Describe the morphology of the erythrocytes.
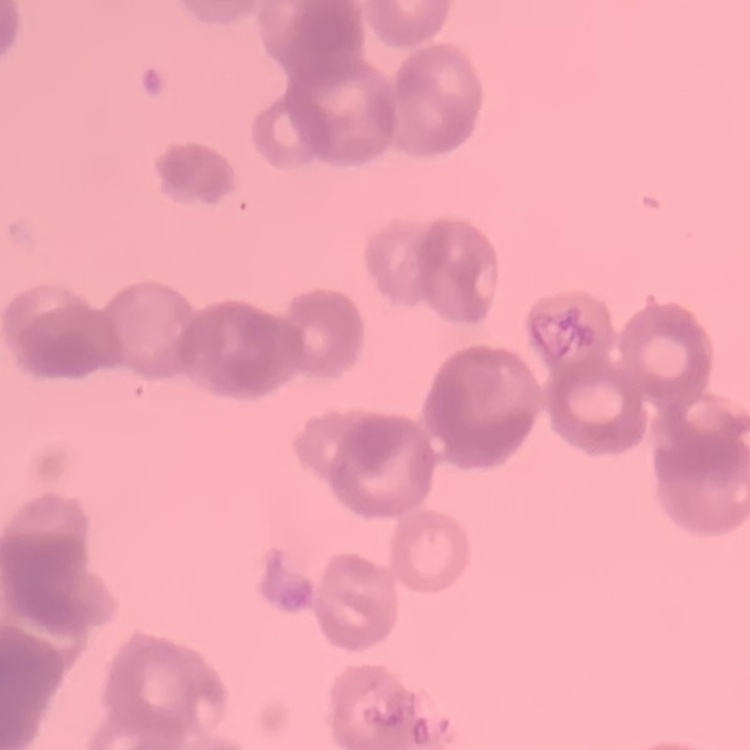

Rouleaux formation.

Thin blood smear. Square crop of a larger photomicrograph. Stained with either Field's or Giemsa.